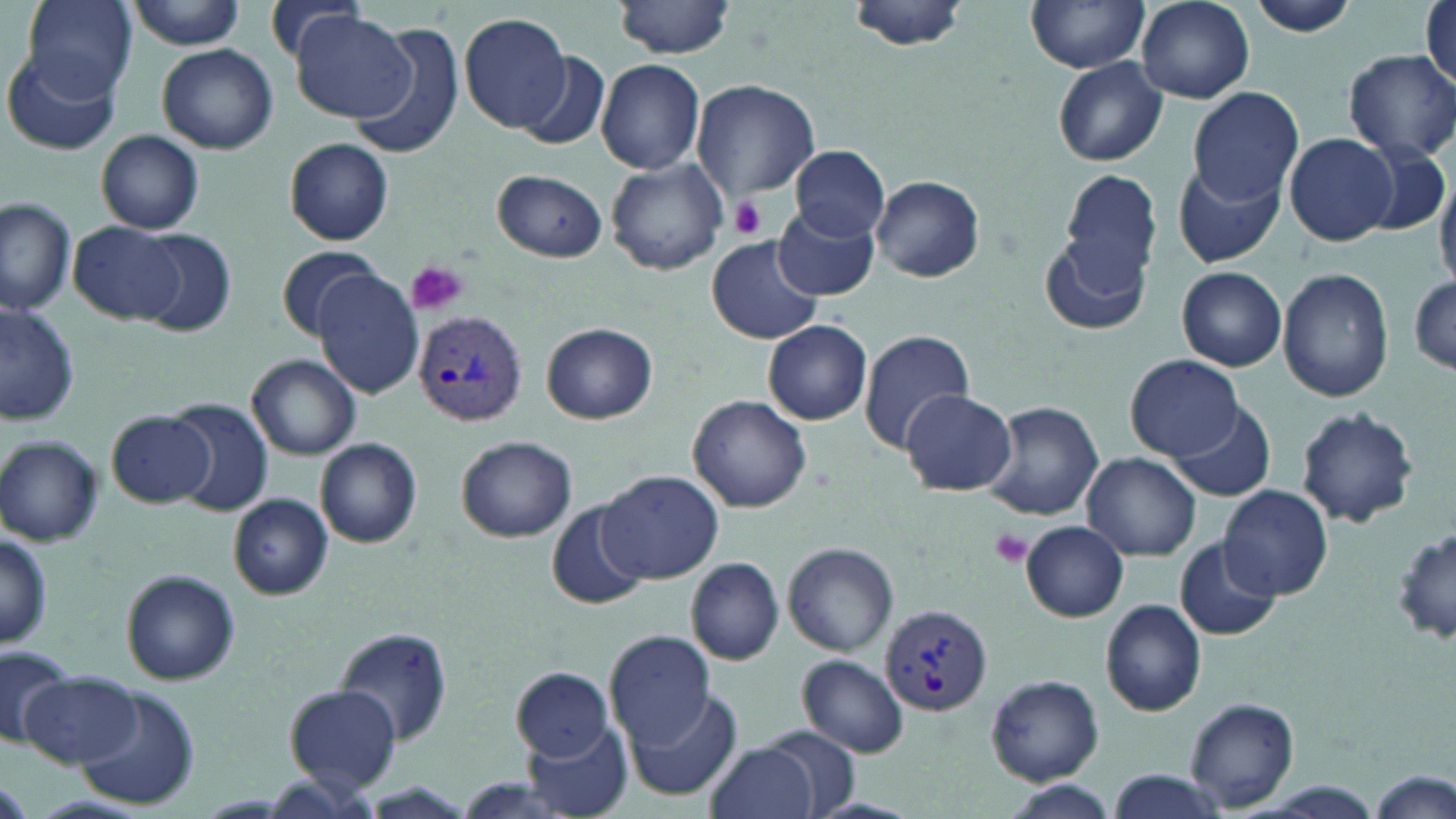
Summary:
  - Coordinate format: approximate bounding boxes as (x1, y1, x2, y2) in pixels
  - Platelet locations: (729, 194, 767, 238), (406, 260, 469, 316), (989, 527, 1034, 567)
  - Plasmodium vivax-infected red blood cell locations: (411, 310, 527, 426), (881, 604, 992, 714)
  - Uninfected red blood cell locations: (26, 0, 139, 104), (848, 0, 973, 53), (1026, 0, 1150, 73), (1244, 0, 1363, 36), (260, 1, 370, 69), (614, 1, 737, 58), (1137, 1, 1253, 103), (1421, 1, 1455, 95), (130, 2, 249, 50), (289, 10, 419, 125), (459, 12, 573, 132), (1088, 15, 1248, 143), (344, 23, 468, 160), (157, 43, 278, 154), (2, 49, 119, 156), (1342, 49, 1456, 165), (518, 52, 609, 150), (1052, 57, 1168, 166), (596, 59, 704, 175), (692, 80, 820, 203), (1186, 85, 1304, 205), (96, 130, 205, 235), (1283, 133, 1393, 246), (285, 138, 394, 245), (1355, 141, 1449, 240), (792, 146, 891, 242), (607, 159, 728, 275), (1171, 160, 1283, 267), (1061, 168, 1162, 281), (1435, 168, 1456, 284), (492, 169, 607, 263), (873, 178, 984, 281), (0, 196, 77, 315), (772, 204, 878, 300), (70, 222, 187, 324), (133, 229, 237, 338), (1040, 232, 1153, 338), (707, 237, 823, 345), (277, 245, 386, 340), (1176, 266, 1286, 371), (1279, 269, 1394, 402), (314, 270, 427, 398), (1409, 275, 1456, 375), (1, 300, 80, 425), (763, 320, 872, 426), (541, 323, 657, 424), (857, 329, 976, 451), (247, 354, 361, 460), (1127, 355, 1242, 459), (899, 390, 1015, 494), (688, 395, 812, 513), (168, 398, 274, 516), (981, 399, 1103, 521), (1164, 404, 1275, 502), (1296, 407, 1421, 529), (106, 409, 214, 508), (0, 434, 104, 546), (455, 435, 577, 543), (316, 439, 422, 547), (1082, 452, 1200, 560), (598, 468, 725, 585), (1219, 485, 1333, 601), (229, 495, 332, 598), (549, 501, 651, 611), (1023, 521, 1128, 620), (1394, 526, 1456, 646), (0, 531, 53, 648), (1175, 540, 1280, 641), (783, 541, 897, 657), (686, 557, 783, 665), (122, 570, 242, 686), (1100, 599, 1206, 715), (335, 627, 453, 746), (604, 628, 717, 751), (2, 647, 76, 752), (798, 653, 909, 758), (512, 668, 613, 761), (22, 673, 142, 768), (986, 675, 1104, 784), (626, 685, 742, 801), (285, 686, 401, 793), (72, 688, 198, 808), (1184, 697, 1301, 812), (521, 722, 633, 816), (764, 728, 862, 814), (707, 740, 820, 819), (1368, 768, 1456, 818), (1106, 769, 1232, 817), (1005, 783, 1121, 816), (809, 798, 919, 819)
  - Slide-level diagnosis: Plasmodium vivax
  - Preparation: thin blood smear
  - Modality: optical microscopy
  - Magnification: 1000x
  - Stain: May-Grünwald-Giemsa
  - Image size: 1456×819 pixels
  - Field of view: single